Locate and identify every blood parasite.
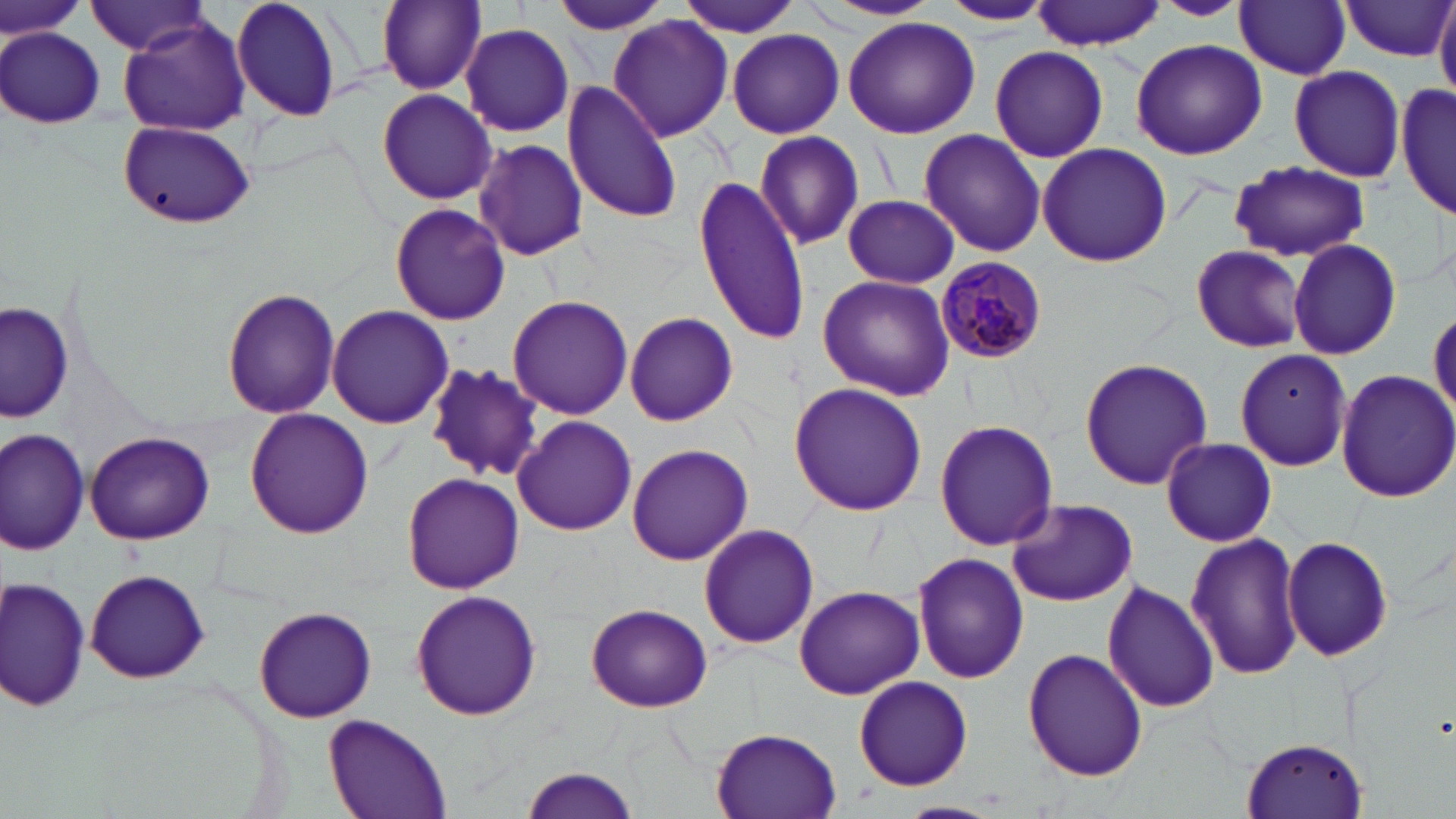
Approximate bounding boxes as [x1, y1, x2, y2] in pixels.
Plasmodium malariae-infected red blood cells: [936, 256, 1049, 361].
No Plasmodium falciparum, Plasmodium ovale, Plasmodium vivax, Babesia divergens, or Trypanosoma brucei observed.

Uninfected red blood cell locations: [0, 0, 87, 45], [231, 0, 346, 124], [375, 0, 486, 93], [677, 0, 804, 40], [821, 0, 943, 22], [1155, 0, 1249, 21], [936, 1, 1057, 28], [1032, 1, 1167, 50], [1236, 1, 1352, 79], [550, 2, 673, 37], [1340, 2, 1452, 60], [1434, 2, 1456, 104], [86, 3, 213, 57], [608, 15, 735, 141], [843, 18, 981, 138], [119, 19, 252, 137], [460, 23, 573, 136], [2, 28, 106, 129], [728, 29, 844, 138], [1129, 38, 1267, 160], [988, 45, 1109, 165], [1288, 66, 1406, 183], [562, 81, 681, 223], [1396, 82, 1455, 219], [377, 87, 495, 205], [118, 120, 255, 229], [918, 130, 1047, 257], [754, 131, 865, 251], [473, 139, 590, 261], [1037, 142, 1171, 267], [1230, 161, 1371, 261], [693, 174, 810, 347], [844, 195, 960, 288], [389, 204, 511, 324], [1286, 240, 1402, 360], [1190, 244, 1309, 352], [816, 273, 955, 400], [221, 286, 340, 417], [507, 295, 633, 420], [1, 301, 74, 424], [326, 304, 453, 429], [1429, 306, 1455, 424], [624, 311, 738, 426], [1234, 349, 1351, 471], [1080, 356, 1212, 490], [425, 363, 543, 479], [1331, 368, 1456, 503], [789, 382, 926, 517], [243, 409, 374, 540], [512, 415, 636, 536], [935, 420, 1058, 551], [1, 429, 89, 556], [84, 431, 215, 546], [1160, 436, 1278, 547], [626, 443, 754, 566], [402, 471, 524, 594], [1008, 499, 1138, 607], [697, 523, 821, 649], [1185, 532, 1307, 681], [1282, 534, 1393, 664], [913, 551, 1029, 685], [84, 570, 209, 683], [2, 575, 93, 713], [1101, 580, 1220, 715], [795, 585, 923, 699], [411, 591, 542, 722], [587, 603, 712, 712], [254, 605, 377, 723], [1021, 646, 1149, 783], [852, 675, 974, 790], [325, 713, 452, 819], [710, 728, 842, 819], [1237, 737, 1370, 819], [520, 765, 642, 819]. Slide-level diagnosis: Plasmodium malariae. Optical microscopy. Thin blood smear. Captured at 1000x magnification. One field of a larger specimen. May-Grünwald-Giemsa-stained preparation. Image is 1456×819 pixels.